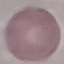
Summary:
  - Malaria status: uninfected
  - Image type: cell patch, automatically extracted from a larger field of view and resized to 64 × 64 pixels
  - Capture: smartphone through the microscope eyepiece
  - Stain: Giemsa
  - Preparation: thin blood smear